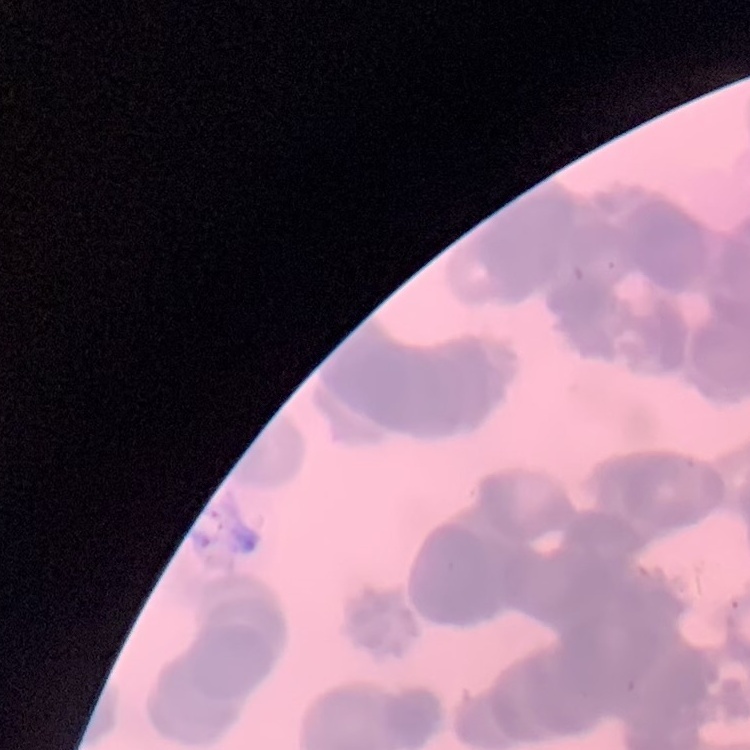

Summary:
  - Red blood cell morphology: rouleaux formation
  - Stain: Field's or Giemsa
  - Image type: one tile cut from a larger photomicrograph
  - Preparation: thin blood film